Name the parasite shown.
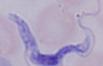
This is a trypanosome.

Summary:
  - Modality: micrograph
  - Magnification: 1000x